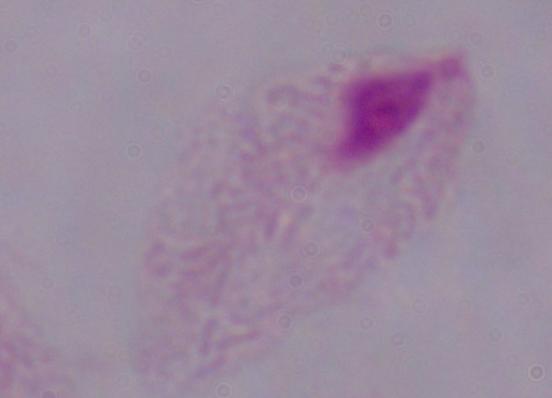

modality: photomicrograph
identification: trichomonad
magnification: 1000x